State which cell type is depicted.
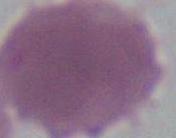

This is an erythrocyte.

Photomicrograph. 1000x magnification.